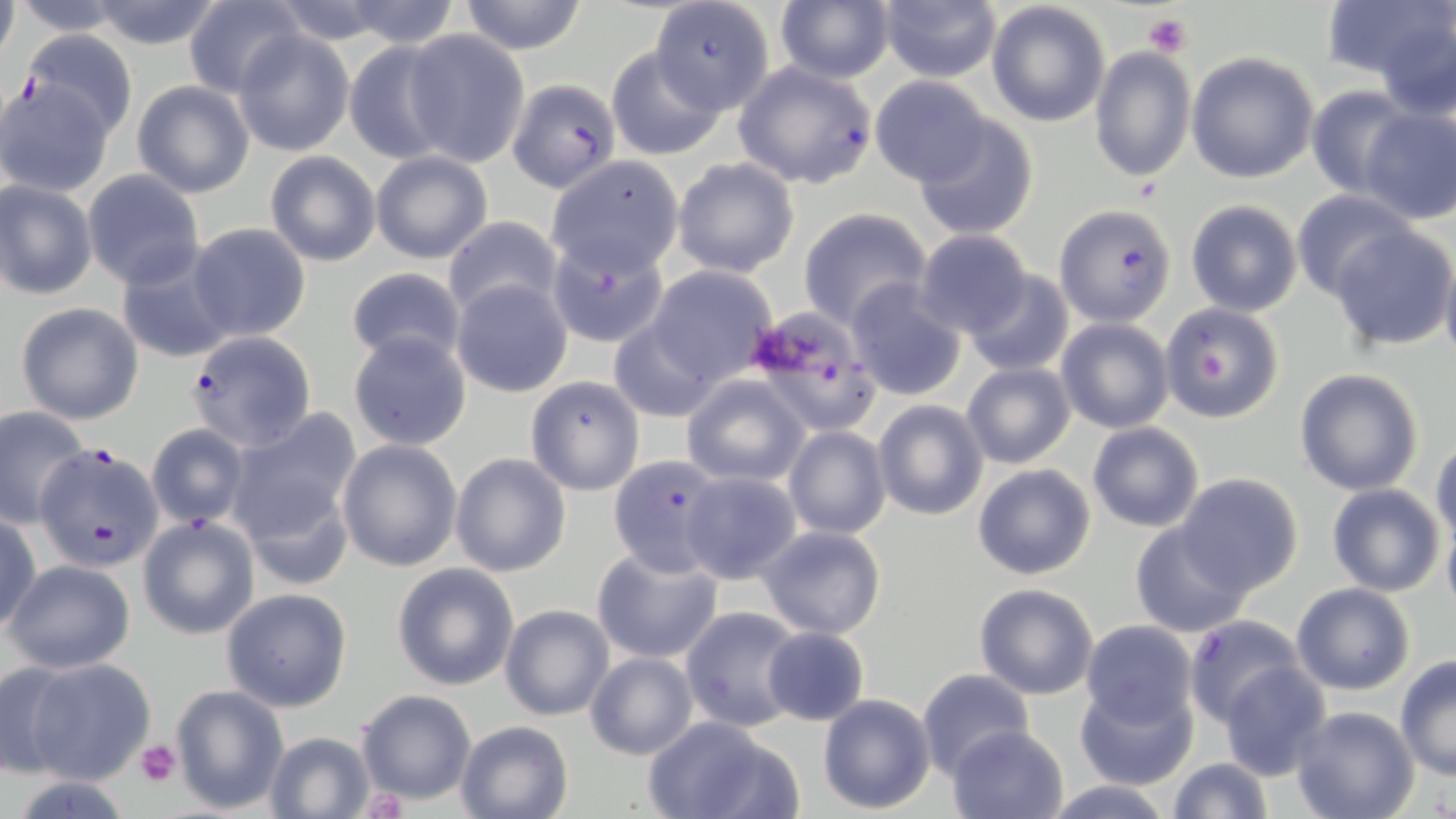

Plasmodium falciparum-infected red blood cell locations = approximate bounding boxes as (x1, y1, x2, y2) in pixels: (652, 0, 775, 110), (18, 31, 138, 141), (734, 61, 877, 188), (507, 77, 621, 193), (1054, 204, 1176, 326), (545, 240, 667, 347), (183, 330, 317, 451), (37, 446, 164, 571), (607, 456, 724, 573), (1185, 615, 1307, 726)
slide-level diagnosis = Plasmodium falciparum
modality = light microscopy
platelet locations = approximate bounding boxes as (x1, y1, x2, y2) in pixels: (1144, 13, 1191, 59), (136, 739, 182, 785)
image size = 1456×819 pixels
preparation = thin blood smear
stain = May-Grünwald-Giemsa
uninfected red blood cell locations = approximate bounding boxes as (x1, y1, x2, y2) in pixels: (0, 0, 19, 66), (85, 0, 226, 50), (457, 0, 589, 54), (1332, 0, 1456, 111), (7, 1, 139, 37), (183, 1, 304, 98), (337, 1, 462, 48), (986, 1, 1111, 126), (773, 2, 895, 83), (878, 2, 1001, 82), (400, 30, 530, 167), (233, 31, 354, 157), (343, 41, 458, 162), (1089, 45, 1194, 183), (606, 47, 725, 160), (1186, 52, 1319, 183), (870, 75, 991, 185), (1, 76, 116, 196), (131, 81, 254, 198), (1306, 86, 1414, 196), (1359, 106, 1455, 225), (913, 115, 1038, 240), (369, 150, 493, 265), (264, 151, 380, 267), (545, 156, 683, 276), (672, 158, 799, 277), (83, 170, 207, 288), (1, 180, 98, 300), (1291, 190, 1418, 305), (1186, 199, 1303, 317), (798, 209, 931, 329), (443, 217, 564, 322), (186, 224, 311, 343), (1329, 225, 1455, 350), (913, 230, 1032, 337), (116, 250, 236, 366), (1440, 254, 1456, 372), (647, 266, 777, 385), (345, 267, 467, 369), (963, 271, 1074, 376), (451, 278, 573, 397), (844, 279, 969, 401), (14, 301, 144, 424), (1161, 303, 1286, 423), (761, 307, 875, 434), (607, 318, 724, 421), (1056, 318, 1173, 433), (348, 332, 472, 449), (961, 361, 1076, 470), (1293, 367, 1424, 496), (682, 375, 809, 486), (525, 376, 645, 496), (873, 399, 988, 521), (0, 405, 92, 527), (229, 408, 362, 540), (1087, 422, 1204, 531), (145, 423, 248, 528), (783, 425, 891, 541), (1431, 435, 1456, 547), (337, 438, 463, 572), (450, 452, 572, 577), (973, 463, 1096, 580), (681, 471, 802, 583), (1176, 472, 1305, 595), (1326, 483, 1446, 596), (1, 511, 41, 636), (137, 515, 260, 639), (1442, 518, 1456, 618), (1130, 519, 1254, 637), (757, 525, 887, 639), (591, 546, 722, 665), (4, 557, 134, 674), (391, 563, 520, 690), (974, 582, 1100, 700), (1290, 582, 1416, 696), (220, 588, 353, 713), (499, 603, 614, 721), (681, 607, 803, 731), (1080, 619, 1197, 728), (761, 626, 870, 726), (584, 651, 698, 759), (1393, 657, 1456, 780), (25, 658, 155, 784), (0, 662, 81, 778), (1217, 663, 1331, 779), (917, 668, 1037, 777), (1074, 681, 1199, 789), (171, 685, 288, 811), (355, 688, 477, 805), (816, 693, 937, 814), (1291, 706, 1419, 819), (640, 714, 794, 819), (454, 720, 574, 819), (947, 724, 1069, 818), (263, 731, 379, 819), (1167, 757, 1273, 819), (1042, 778, 1177, 818)
magnification = 1000x
field of view = single